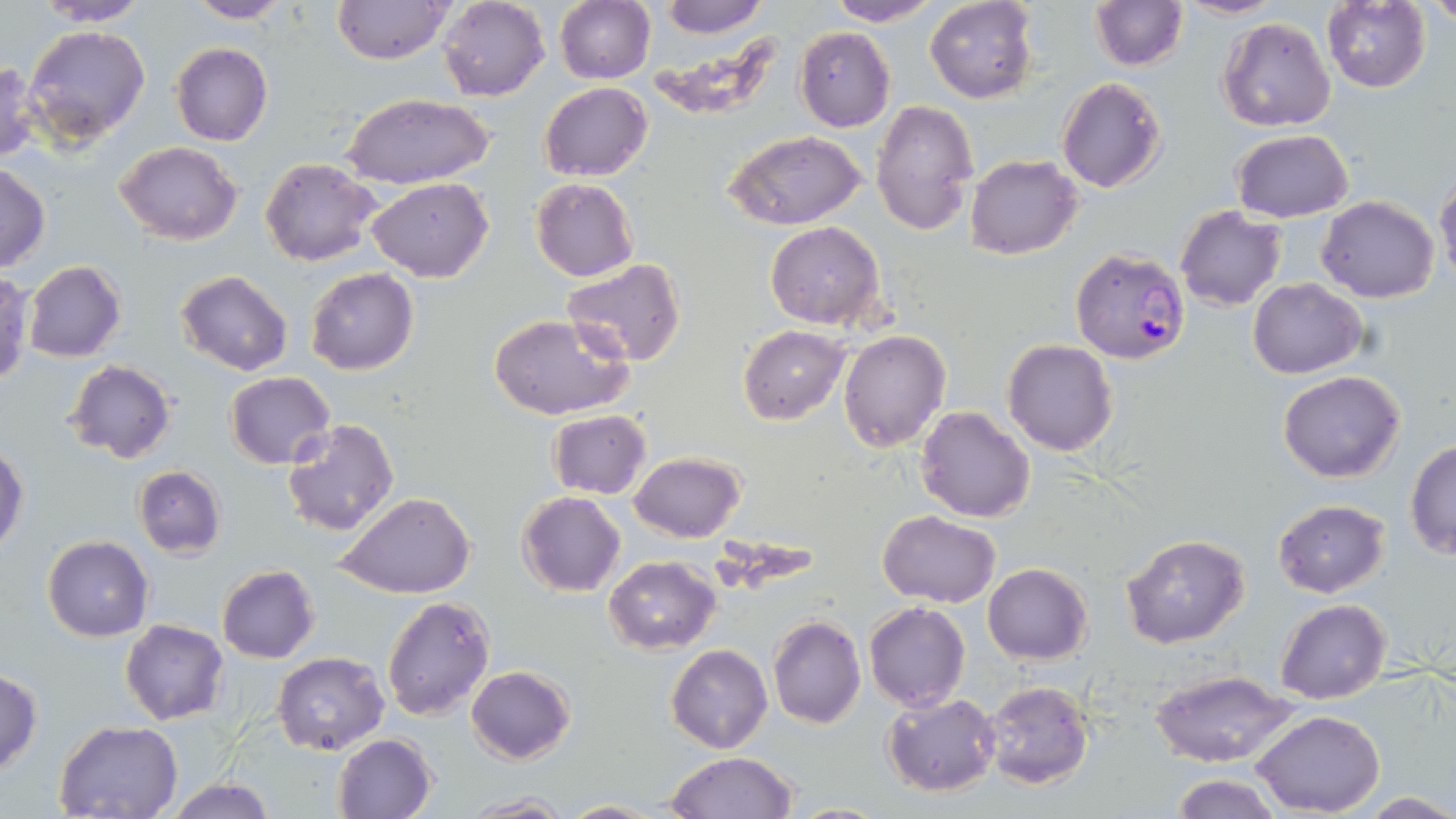
Plasmodium falciparum-infected red blood cell locations = approximate bounding boxes as [x1, y1, x2, y2] in pixels: [1064, 245, 1190, 377]
slide-level diagnosis = Plasmodium falciparum
magnification = 1000x
uninfected red blood cell locations = approximate bounding boxes as [x1, y1, x2, y2] in pixels: [32, 0, 153, 25], [437, 0, 551, 101], [554, 0, 655, 85], [661, 0, 768, 38], [824, 0, 943, 26], [925, 0, 1037, 103], [1172, 0, 1283, 20], [1429, 0, 1456, 28], [184, 1, 294, 23], [332, 1, 454, 66], [1090, 1, 1187, 71], [1321, 1, 1432, 93], [1217, 17, 1336, 133], [22, 23, 152, 148], [795, 27, 895, 131], [170, 43, 273, 147], [0, 61, 41, 165], [1056, 77, 1167, 194], [538, 82, 652, 181], [340, 94, 493, 189], [872, 100, 978, 235], [1231, 129, 1352, 223], [723, 130, 867, 231], [113, 140, 242, 245], [964, 154, 1083, 258], [260, 156, 383, 267], [0, 162, 50, 273], [1435, 172, 1456, 291], [531, 177, 638, 282], [367, 179, 492, 283], [1317, 196, 1440, 303], [1176, 206, 1286, 311], [762, 221, 887, 330], [561, 259, 688, 368], [23, 262, 126, 362], [304, 267, 419, 376], [175, 269, 292, 376], [0, 272, 33, 386], [1248, 278, 1366, 378], [491, 315, 630, 422], [739, 326, 851, 423], [838, 329, 951, 453], [1003, 339, 1118, 456], [63, 360, 178, 463], [1278, 370, 1406, 483], [225, 371, 336, 468], [916, 405, 1035, 522], [546, 410, 651, 499], [281, 418, 398, 536], [1404, 439, 1456, 561], [0, 446, 28, 554], [631, 451, 744, 542], [133, 466, 225, 559], [517, 492, 626, 597], [336, 493, 477, 600], [1272, 500, 1391, 598], [880, 512, 1000, 607], [1120, 534, 1250, 648], [43, 535, 152, 641], [604, 556, 721, 653], [983, 563, 1093, 664], [217, 565, 319, 664], [382, 593, 495, 720], [1276, 598, 1391, 704], [865, 602, 969, 711], [767, 616, 865, 728], [120, 619, 228, 724], [666, 643, 772, 754], [272, 651, 389, 755], [465, 666, 575, 764], [0, 670, 43, 775], [1150, 670, 1296, 768], [980, 680, 1095, 789], [882, 692, 1001, 796], [1252, 710, 1384, 816], [55, 720, 185, 817], [332, 733, 437, 818], [663, 751, 799, 818], [1171, 774, 1281, 819], [164, 777, 276, 819], [462, 792, 574, 818], [1360, 792, 1456, 817], [561, 798, 665, 817]
preparation = thin blood film
image size = 1456×819 pixels
modality = optical microscopy
stain = May-Grünwald-Giemsa
field of view = one of a larger specimen